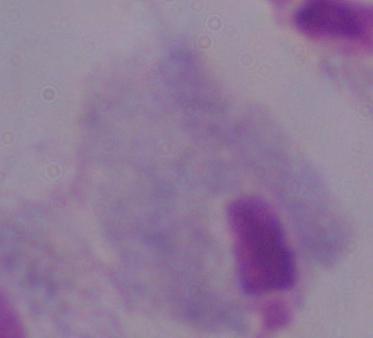 1000x magnification. A trichomonad is seen. Photomicrograph.